Classify this cell by malaria status.
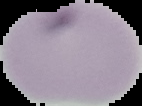

It is uninfected.

Summary:
  - Image type: cell region segmented out of the field of view; surrounding area masked to black
  - Preparation: thin blood film
  - Image size: 142×106 pixels